Name the parasite shown.
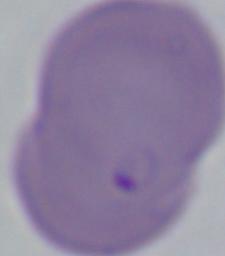
Babesia.

1000x magnification. Micrograph.